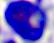

A leukocyte is seen. Micrograph. 400x magnification.